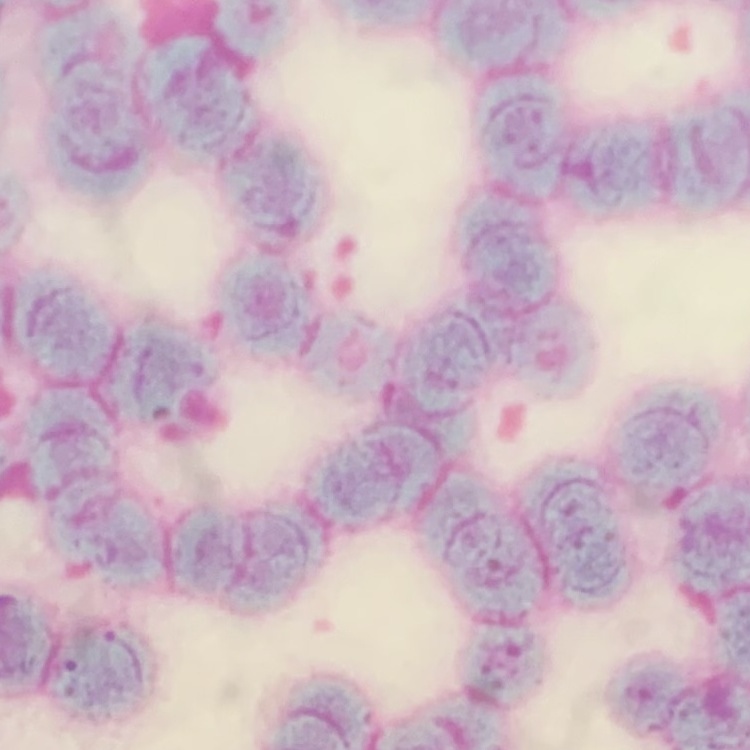
The erythrocytes exhibit rouleaux formation. One tile cut from a larger photomicrograph. Thin peripheral smear. Field's or Giemsa stain.